Identify the parasite.
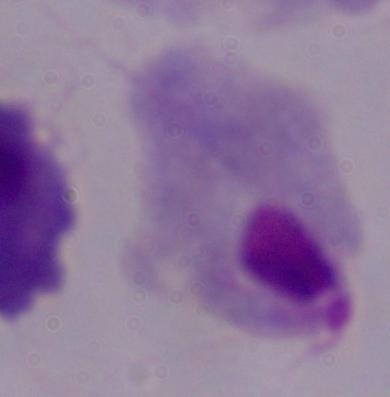

This is a trichomonad.

Summary:
  - Modality: photomicrograph
  - Magnification: 1000x